Assess this cell for malaria.
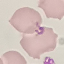
Uninfected.

Photographed with a smartphone camera at the microscope eyepiece. Giemsa-stained preparation. Automatically extracted cell patch, resized to 64 × 64 pixels. Thin smear of blood.